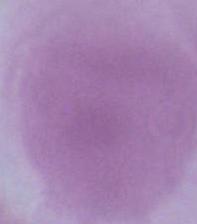
magnification = 1000x
modality = photomicrograph
identification = erythrocyte